Assess this cell for malaria.
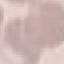

It is uninfected.

Summary:
  - Preparation: thin smear
  - Stain: Giemsa
  - Image type: automatically extracted cell patch, resized to 64 × 64 pixels
  - Capture: smartphone camera at the microscope eyepiece